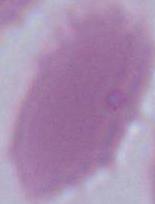
identification = red blood cell
magnification = 1000x
modality = micrograph